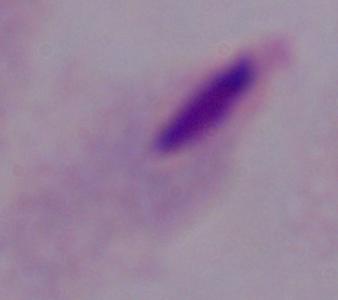

Summary:
  - Magnification: 1000x
  - Identification: trichomonad
  - Modality: micrograph